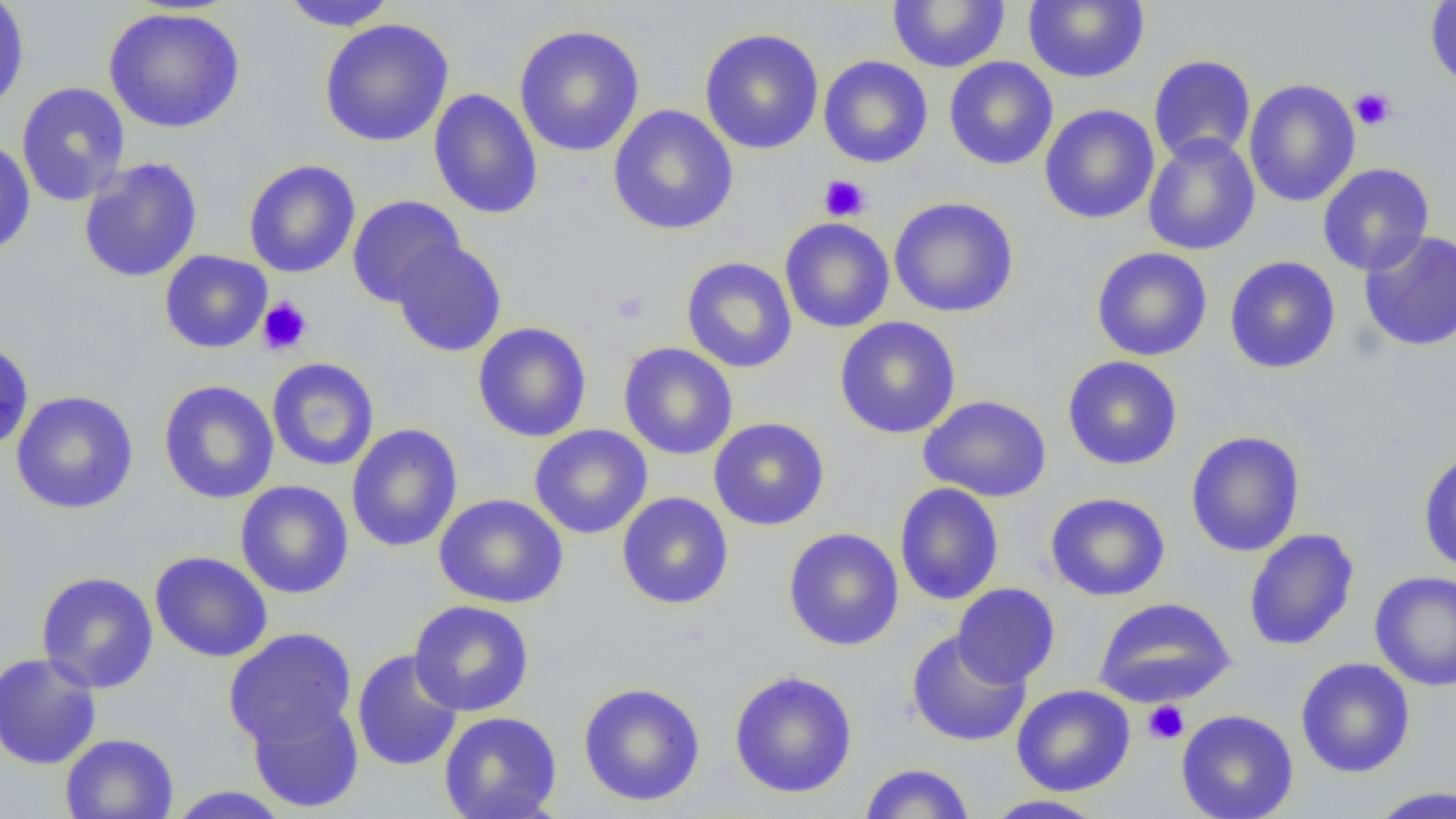 Approximate bounding boxes as [x1, y1, x2, y2] in pixels. Uninfected red blood cell locations: [0, 0, 30, 113], [279, 0, 399, 31], [887, 0, 1010, 72], [1425, 0, 1456, 91], [1022, 1, 1150, 84], [103, 8, 245, 133], [319, 18, 454, 147], [514, 24, 645, 157], [699, 28, 824, 155], [1148, 54, 1256, 165], [818, 55, 933, 168], [943, 56, 1058, 171], [1243, 78, 1360, 207], [16, 82, 131, 206], [428, 88, 543, 220], [1039, 104, 1160, 224], [607, 105, 738, 235], [1142, 134, 1260, 256], [0, 139, 36, 257], [78, 158, 203, 283], [243, 159, 361, 278], [1317, 162, 1435, 276], [346, 196, 465, 307], [888, 196, 1019, 318], [779, 217, 895, 333], [1359, 230, 1456, 352], [391, 239, 507, 357], [1091, 247, 1212, 361], [159, 250, 272, 354], [1224, 256, 1341, 374], [681, 257, 798, 373], [834, 316, 961, 439], [472, 322, 592, 442], [0, 339, 34, 453], [618, 342, 738, 460], [1062, 356, 1183, 470], [267, 358, 379, 471], [158, 380, 279, 504], [11, 390, 139, 514], [918, 395, 1053, 502], [708, 417, 830, 531], [346, 424, 463, 553], [529, 425, 653, 539], [1185, 430, 1305, 557], [1418, 449, 1456, 573], [234, 481, 354, 599], [894, 482, 1004, 606], [616, 491, 734, 610], [1045, 492, 1171, 601], [434, 493, 568, 608], [783, 527, 904, 651], [1243, 528, 1360, 651], [149, 551, 273, 662], [1369, 570, 1456, 691], [36, 571, 158, 694], [952, 583, 1061, 687], [1093, 597, 1235, 707], [409, 599, 534, 716], [223, 627, 357, 749], [905, 629, 1032, 748], [351, 649, 464, 771], [0, 652, 102, 770], [1295, 657, 1416, 778], [729, 670, 858, 799], [578, 682, 706, 807], [1011, 684, 1135, 796], [247, 699, 364, 814], [1176, 709, 1299, 819], [438, 711, 563, 819], [60, 733, 178, 819], [858, 762, 976, 818], [1365, 785, 1456, 818], [164, 786, 293, 818], [982, 794, 1106, 818]. Platelet locations: [1350, 88, 1396, 131], [819, 174, 871, 222], [611, 290, 650, 324], [257, 296, 313, 356], [1142, 700, 1189, 745]. Slide-level diagnosis: no evidence of blood parasites. Image is 1456×819 pixels. Light microscopy. Thin blood smear. Single field of view. Captured at 1000x magnification.